Assess this cell for malaria.
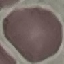

Uninfected.

capture = smartphone through the microscope eyepiece
preparation = thin blood smear
image type = automatically extracted cell patch, resized to 64 × 64 pixels
stain = Giemsa